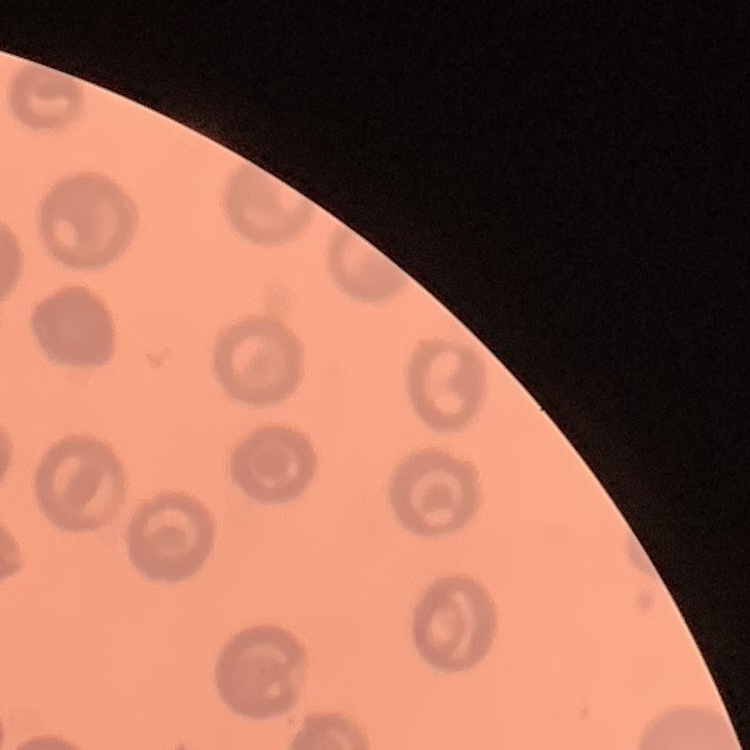

Summary:
  - Erythrocyte morphology: no rouleaux formation
  - Preparation: thin blood film
  - Stain: Field's or Giemsa
  - Image type: square crop of a larger photomicrograph